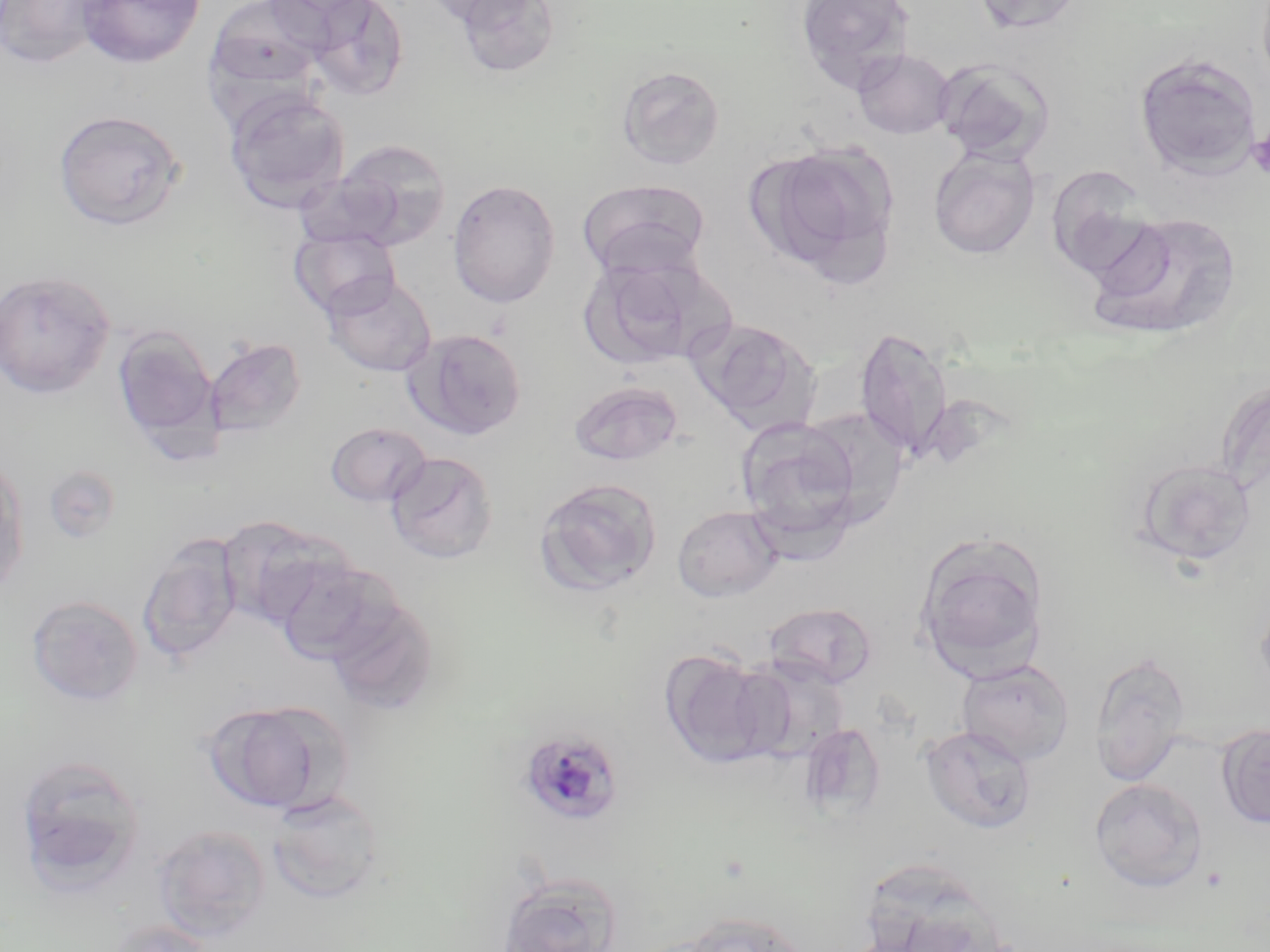 Approximate bounding boxes as [x1, y1, x2, y2] in pixels. Platelet locations: [1246, 129, 1270, 178]. Uninfected red blood cell locations: [0, 0, 113, 69], [78, 0, 205, 69], [262, 0, 380, 43], [306, 0, 410, 100], [418, 0, 540, 27], [453, 0, 561, 80], [795, 0, 915, 93], [970, 0, 1085, 36], [205, 1, 326, 96], [852, 48, 956, 139], [1133, 53, 1262, 180], [933, 56, 1056, 165], [617, 65, 725, 170], [224, 89, 350, 213], [53, 109, 187, 231], [330, 138, 451, 249], [756, 142, 897, 274], [928, 146, 1041, 259], [1045, 164, 1157, 278], [447, 178, 561, 308], [578, 178, 711, 280], [1085, 210, 1243, 341], [289, 227, 400, 319], [578, 254, 713, 370], [0, 269, 115, 398], [321, 273, 437, 377], [689, 317, 821, 434], [112, 324, 219, 448], [853, 325, 954, 462], [404, 328, 528, 440], [204, 337, 307, 438], [569, 381, 684, 466], [799, 406, 911, 526], [735, 417, 864, 550], [326, 422, 432, 507], [385, 450, 499, 564], [0, 453, 30, 599], [1132, 457, 1257, 567], [43, 464, 122, 544], [535, 477, 663, 597], [672, 505, 783, 602], [216, 516, 339, 628], [915, 532, 1050, 680], [137, 533, 244, 666], [271, 556, 398, 665], [1255, 587, 1270, 702], [26, 595, 144, 706], [324, 596, 439, 714], [762, 602, 878, 689], [658, 649, 779, 769], [1089, 649, 1192, 786], [735, 655, 853, 763], [956, 658, 1074, 766], [201, 699, 346, 814], [799, 722, 887, 821], [1217, 723, 1270, 828], [920, 724, 1037, 834], [14, 753, 147, 890], [1089, 778, 1208, 892], [267, 789, 386, 904], [152, 823, 272, 942], [495, 871, 624, 952], [665, 908, 815, 952], [104, 919, 218, 952]. Plasmodium malariae-infected red blood cell locations: [517, 727, 624, 827]. Slide-level diagnosis: Plasmodium malariae. Optical microscopy. Image is 1270×952 pixels. Single field of view. Thin blood film. May-Grünwald-Giemsa stain. Captured at 1000x magnification.